State which parasite is depicted.
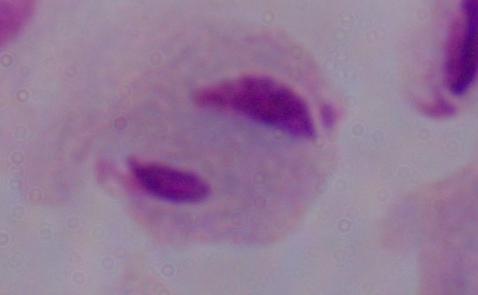
This is a trichomonad.

Captured at 1000x magnification. Photomicrograph.